Identify the parasite.
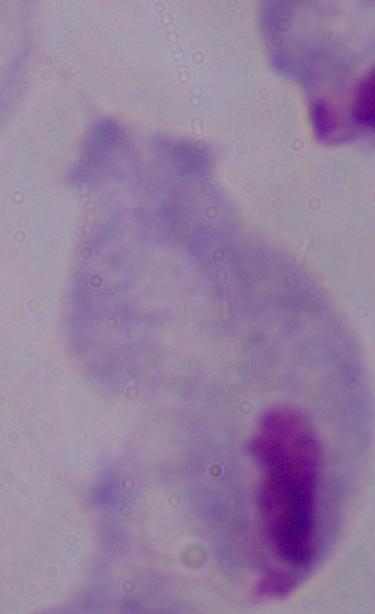

A trichomonad.

Captured at 1000x magnification. Micrograph.